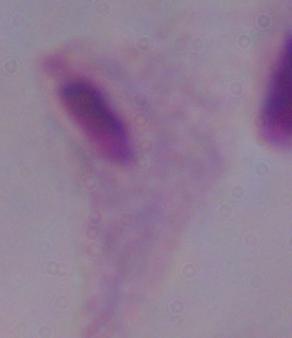
Summary:
  - Identification: trichomonad
  - Magnification: 1000x
  - Modality: photomicrograph